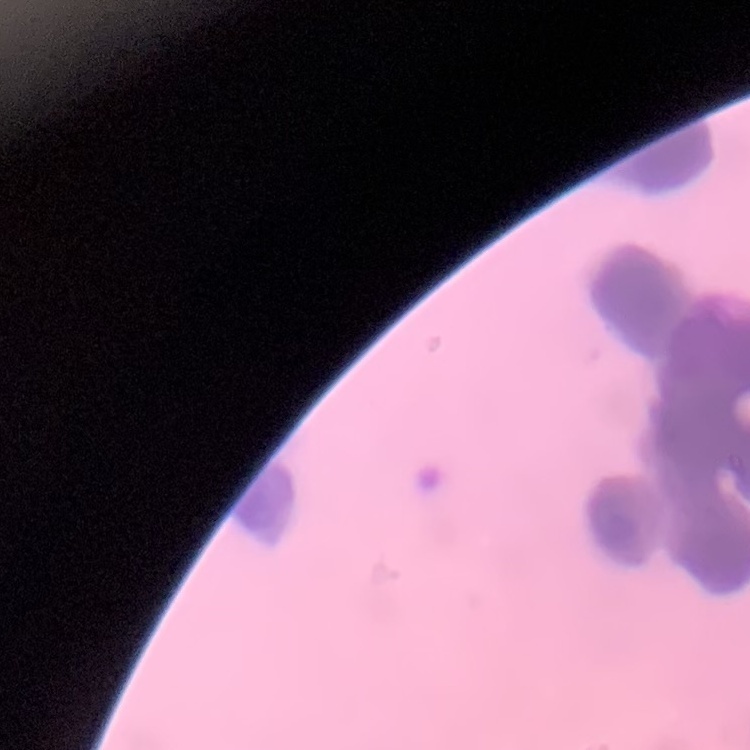

erythrocyte morphology = rouleaux formation
image type = one tile cut from a larger photomicrograph
stain = Field's or Giemsa
preparation = thin peripheral smear